Describe the morphology of the red blood cells.
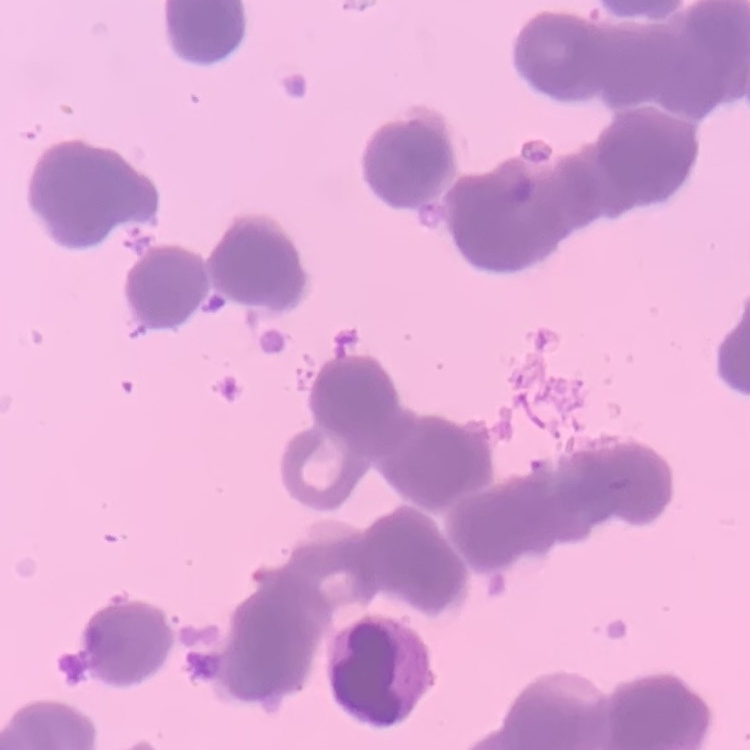
Rouleaux formation.

Thin blood film. Field's or Giemsa stain. Square crop of a larger photomicrograph.